Assess this cell for malaria.
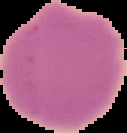
Uninfected.

From a thin blood smear. Cell region segmented out of the field of view; the surrounding area is masked to black. Image is 127×133 pixels.